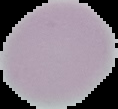
Summary:
  - Image size: 118×109 pixels
  - Preparation: thin blood smear
  - Malaria status: uninfected
  - Image type: segmented cell region on a black background